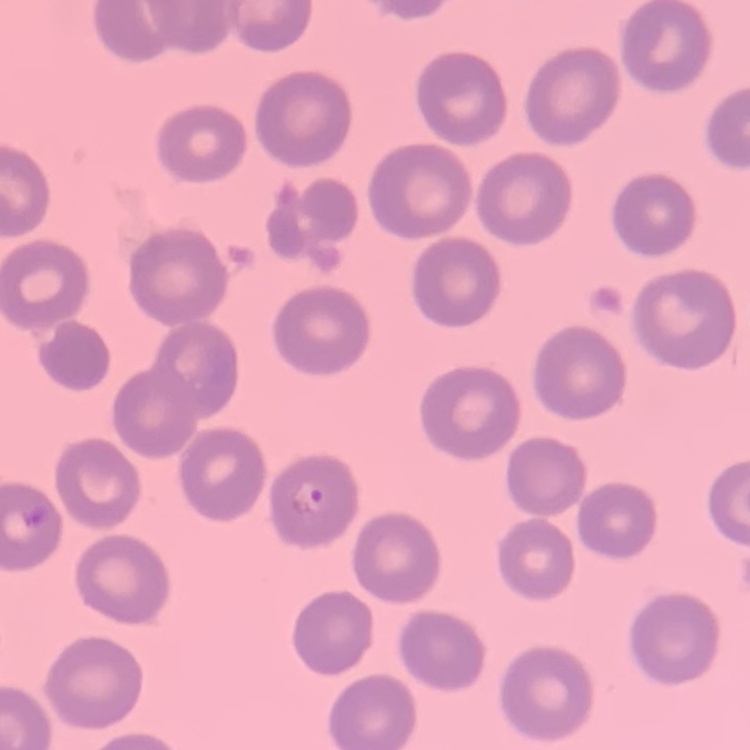

The red blood cells exhibit no rouleaux formation. Thin blood film. One tile cut from a larger photomicrograph. Stained with either Field's or Giemsa.